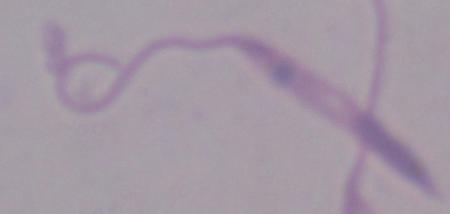
magnification: 1000x
identification: Leishmania
modality: micrograph